Comment on the morphology of the erythrocytes.
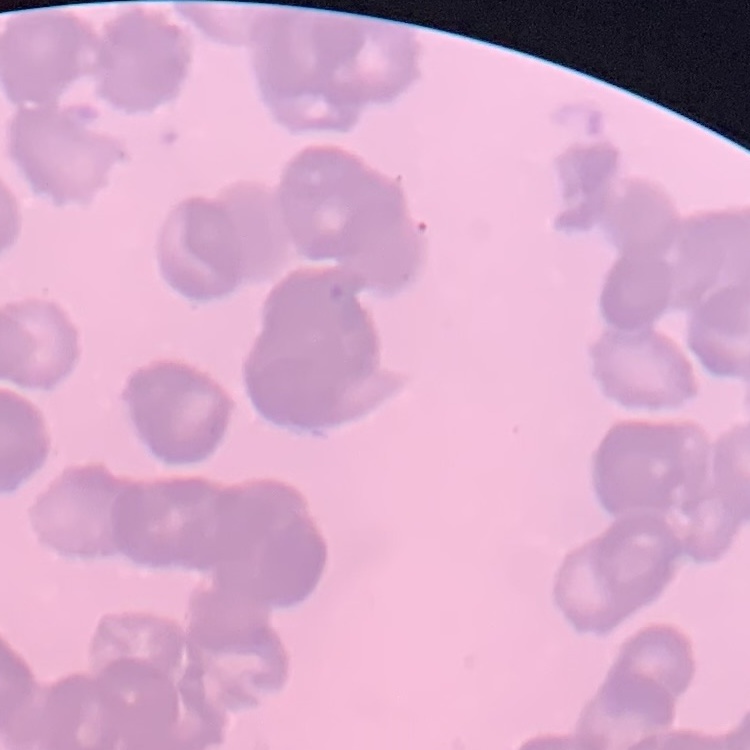

Rouleaux formation.

{
  "stain": "Field's or Giemsa",
  "image_type": "one tile cut from a larger photomicrograph",
  "preparation": "thin blood film"
}